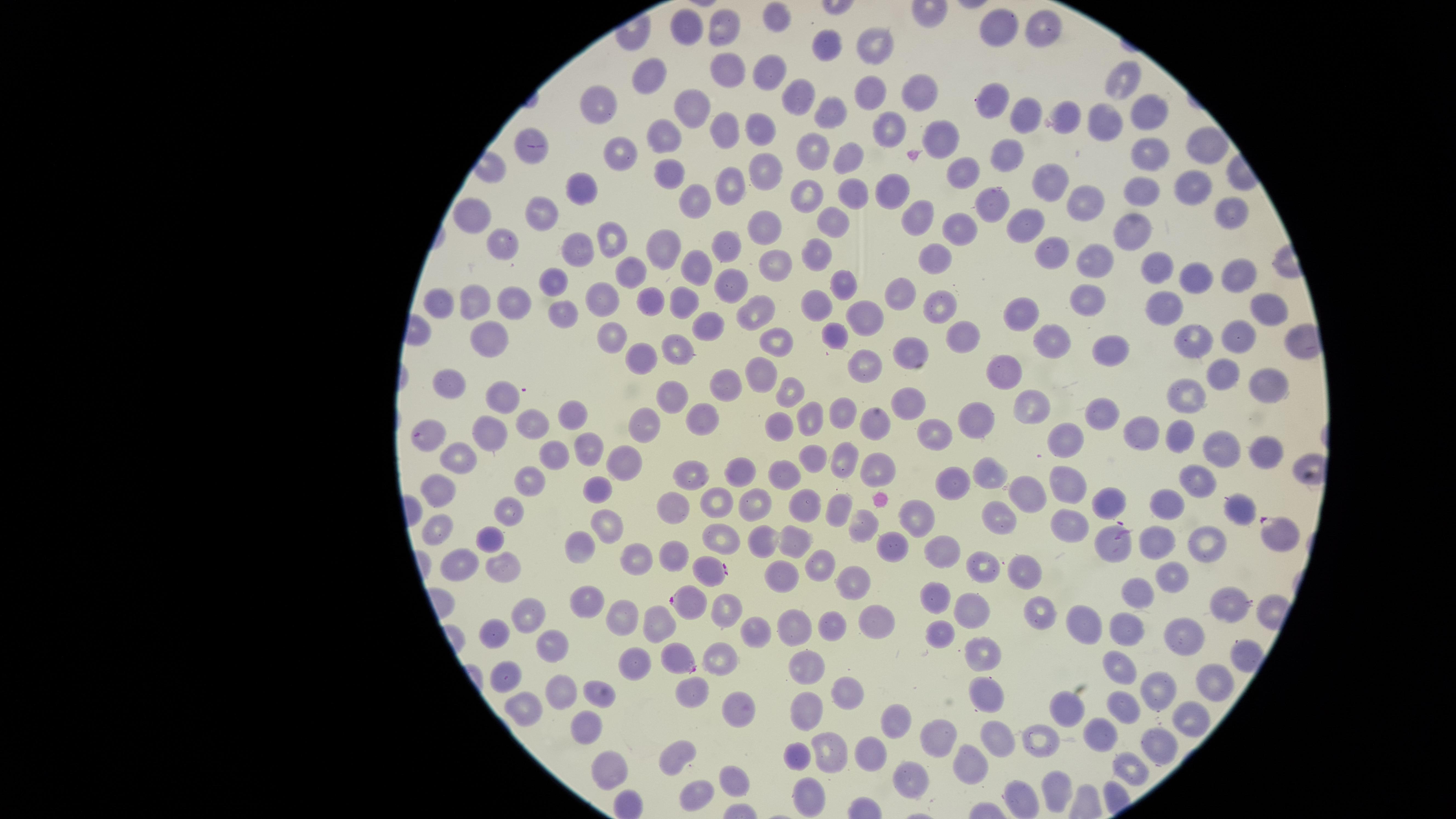

stain = Giemsa
preparation = thin blood film
presence = malaria parasites seen
visible region = circular
species = Plasmodium falciparum
field of view = single
uninfected RBCs = approximate marker points as [x, y] in pixels: [774, 22], [1040, 26], [994, 29], [727, 30], [685, 32], [879, 42], [826, 44], [729, 68], [769, 73], [656, 77], [874, 87], [923, 90], [1116, 90], [793, 98], [1140, 104], [605, 105], [697, 106], [990, 107], [1031, 110], [828, 112], [1062, 113], [1096, 122], [729, 127], [886, 127], [664, 131], [760, 131], [938, 135], [1201, 143], [1151, 151], [816, 153], [619, 155], [842, 157], [1008, 159], [767, 167], [672, 172], [962, 172], [734, 178], [1194, 186], [572, 187], [1054, 188], [1148, 188], [889, 192], [849, 193], [813, 196], [995, 196], [697, 200], [1087, 202], [917, 214], [1229, 215], [476, 216], [538, 218], [762, 223], [831, 224], [960, 227], [1033, 232], [1134, 234], [607, 239], [664, 240], [725, 241], [500, 248], [584, 248], [813, 249], [1051, 252], [932, 253], [1090, 258], [693, 263], [642, 265], [1155, 266], [771, 270], [1241, 271], [1191, 278], [842, 281], [550, 283], [729, 285], [902, 292], [605, 294], [1090, 297], [680, 300], [512, 302], [650, 303], [470, 305], [817, 305], [441, 306], [937, 306], [1266, 306], [1162, 308], [755, 309], [562, 313], [1028, 314], [870, 315], [708, 321], [837, 333], [490, 335], [961, 335], [1241, 335], [1048, 337], [608, 339], [780, 342], [1196, 342], [1108, 348], [906, 349], [671, 354], [641, 355], [866, 358], [762, 371], [1007, 371], [1218, 373], [722, 382], [453, 386], [1270, 387], [789, 391], [1199, 391], [504, 395], [671, 398], [909, 402], [1101, 409], [575, 410], [1034, 410], [840, 413], [699, 416], [811, 419], [975, 420], [535, 424], [777, 426], [644, 427], [872, 428], [1144, 430], [1178, 431], [944, 433], [488, 434], [1068, 446], [1219, 446], [588, 449], [1268, 450], [554, 457], [624, 458], [842, 458], [459, 459], [812, 459], [784, 467], [871, 470], [686, 471], [738, 472], [533, 481], [1193, 481], [992, 483], [952, 486], [1063, 487], [599, 491], [440, 493], [1027, 494], [752, 502], [718, 503], [797, 506], [670, 507], [835, 507], [1109, 507], [1169, 507], [1239, 510], [999, 517], [507, 518], [912, 519], [858, 521], [1068, 523], [439, 525], [609, 529], [789, 537], [487, 539], [722, 539], [763, 540], [1156, 543], [1199, 543], [578, 548], [889, 548], [639, 556], [946, 558], [669, 559], [988, 561], [459, 564], [822, 564], [503, 566], [773, 572], [1024, 575], [1172, 577], [854, 579], [1137, 595], [587, 598], [935, 599], [1230, 599], [975, 611], [523, 615], [720, 615], [625, 617], [654, 619], [1038, 619], [1086, 620], [877, 622], [796, 625], [760, 626], [833, 626], [489, 629], [1124, 631], [1188, 631], [941, 634], [553, 646], [979, 654], [720, 658], [639, 661], [803, 662], [1116, 668], [512, 679], [1211, 683], [839, 685], [1156, 687], [562, 689], [686, 689], [977, 689], [597, 695], [520, 703], [726, 703], [1122, 707], [810, 708], [1062, 708], [895, 715], [1187, 723], [585, 728], [1099, 734], [936, 736], [996, 736], [1042, 740], [1157, 746], [827, 747], [675, 750], [796, 753], [867, 753], [968, 765], [613, 768], [1134, 770], [734, 773], [1060, 791], [807, 793], [695, 799]
image size = 1456×819 pixels
capture = smartphone photograph through the microscope eyepiece
parasitized RBCs = approximate marker points as [x, y] in pixels: [535, 145], [430, 437], [1282, 531], [1117, 543], [710, 571], [688, 600], [679, 658]